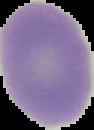
Result: no malaria parasites seen. Image is 94×130 pixels. From a thin blood smear. The area outside the segmented cell region is set to black.